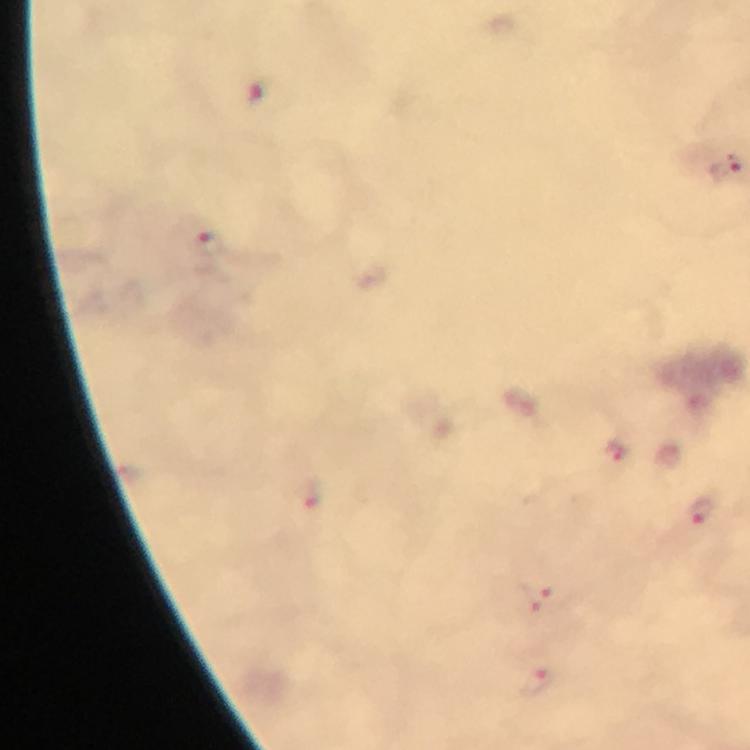
Approximate centers as [x, y] in pixels. Plasmodium parasite locations: [207, 243], [617, 454], [701, 509], [540, 601], [537, 682]. A crop from one field of view. 100x magnification. Photographed with a smartphone mounted on the microscope. From a diagnostic examination for malaria. Immersion oil applied. Image is 750×750 pixels. Giemsa stain. Thick smear.